State the blood parasite species.
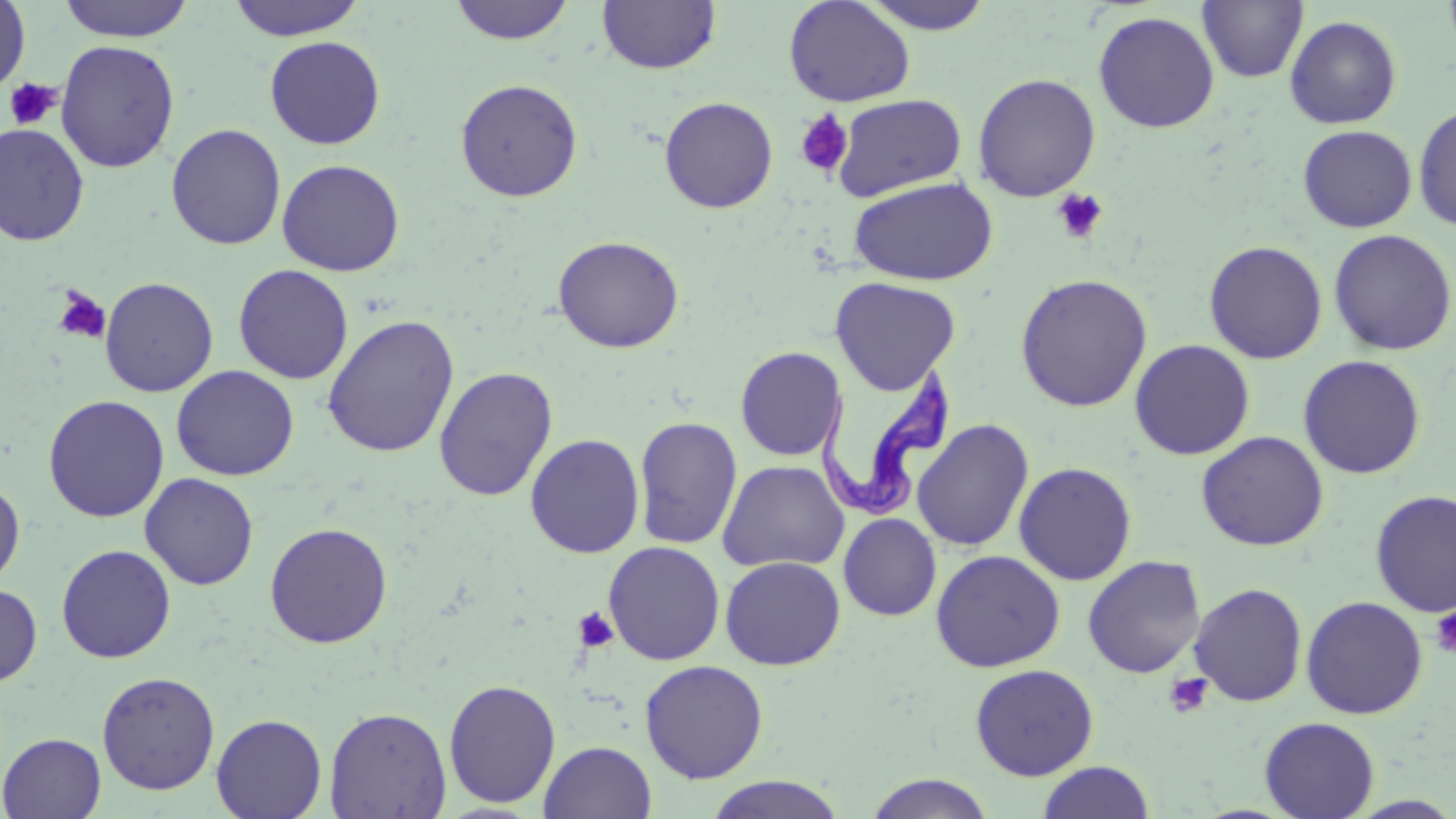
Trypanosoma brucei.

Approximate bounding boxes as (x1,y1)-(x2,y2) corner pairs in pixels. Uninfected red blood cell locations: (0,0)-(31,97), (57,0)-(195,42), (226,0)-(366,41), (449,0)-(576,45), (597,0)-(722,75), (783,0)-(916,107), (861,0)-(996,34), (1197,0)-(1308,83), (1093,11)-(1220,133), (1284,14)-(1402,129), (264,35)-(386,150), (270,36)-(397,271), (55,39)-(180,173), (972,73)-(1101,202), (455,78)-(584,202), (832,94)-(966,201), (659,96)-(778,213), (1413,102)-(1456,232), (0,122)-(90,246), (166,123)-(287,251), (1297,125)-(1417,233), (276,158)-(405,277), (847,176)-(998,286), (1328,228)-(1455,356), (552,235)-(685,353), (1204,240)-(1328,364), (232,264)-(354,384), (1015,273)-(1153,412), (99,276)-(219,397), (830,276)-(961,395), (322,315)-(460,458), (1129,339)-(1255,461), (735,346)-(847,461), (1297,355)-(1426,479), (171,365)-(299,481), (433,366)-(559,501), (43,395)-(169,523), (634,416)-(742,550), (912,418)-(1034,552), (1196,431)-(1329,551), (525,433)-(645,559), (717,459)-(849,573), (1013,461)-(1137,585), (139,473)-(259,590), (0,476)-(25,590), (1370,489)-(1456,618), (838,513)-(942,621), (264,521)-(393,648), (603,541)-(726,665), (56,544)-(176,664), (930,549)-(1066,672), (1082,554)-(1206,678), (720,556)-(845,671), (0,582)-(42,687), (1189,582)-(1308,707), (1301,595)-(1428,719), (639,660)-(769,784), (969,663)-(1099,780), (96,671)-(220,795), (443,678)-(562,808), (324,706)-(451,819), (211,713)-(327,819), (1259,716)-(1380,819), (0,733)-(106,818), (539,740)-(657,819), (1037,761)-(1156,819), (864,773)-(996,818), (705,775)-(847,818). Trypanosoma brucei locations: (817,362)-(959,520). Platelet locations: (4,78)-(62,130), (794,110)-(854,178), (1051,188)-(1109,245), (52,287)-(111,345), (573,606)-(619,653), (1429,606)-(1456,658), (1164,673)-(1213,718). Optical microscopy. 1000x magnification. Single field of view. Image is 1456×819 pixels. May-Grünwald-Giemsa-stained preparation. Thin blood smear.